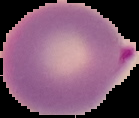
image_type: cell region segmented out of the field of view; surrounding area masked to black
image_size: 139×118 pixels
preparation: thin blood smear
result: Plasmodium parasites identified